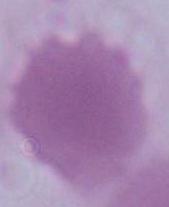

identification = red blood cell
modality = photomicrograph
magnification = 1000x